Assess this cell for malaria.
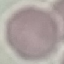

Uninfected.

Summary:
  - Preparation: thin smear
  - Capture: smartphone camera at the microscope eyepiece
  - Image type: automatically extracted cell patch, resized to 64 × 64 pixels
  - Stain: Giemsa